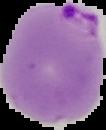

Summary:
  - Result: Plasmodium parasites detected
  - Image size: 106×130 pixels
  - Preparation: thin blood smear
  - Image type: segmented cell region with the area outside set to black